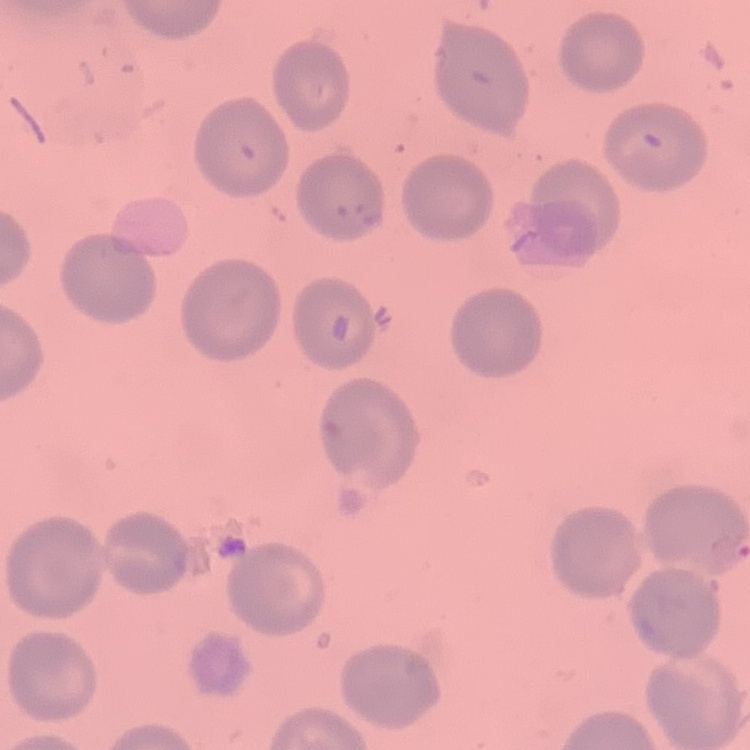
The erythrocytes show no rouleaux formation. Stained with either Field's or Giemsa. Thin blood film. Square crop of a larger photomicrograph.